Assess this cell for malaria.
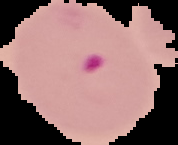

Parasitized.

From a thin blood film. Image is 178×145 pixels. Segmented cell region on a black background.